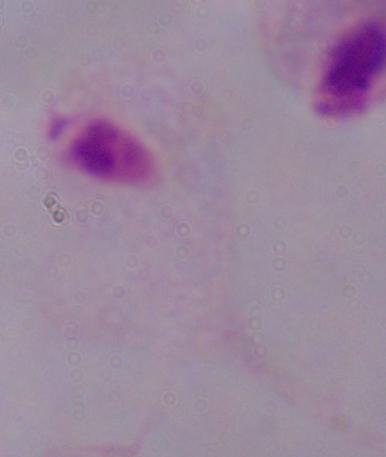

A trichomonad is shown. 1000x magnification. Micrograph.